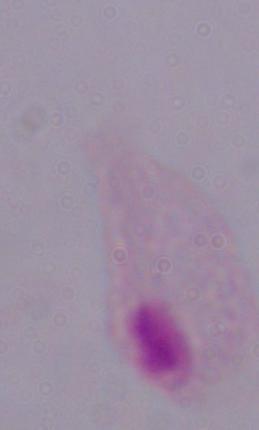

Summary:
  - Modality: photomicrograph
  - Identification: trichomonad
  - Magnification: 1000x